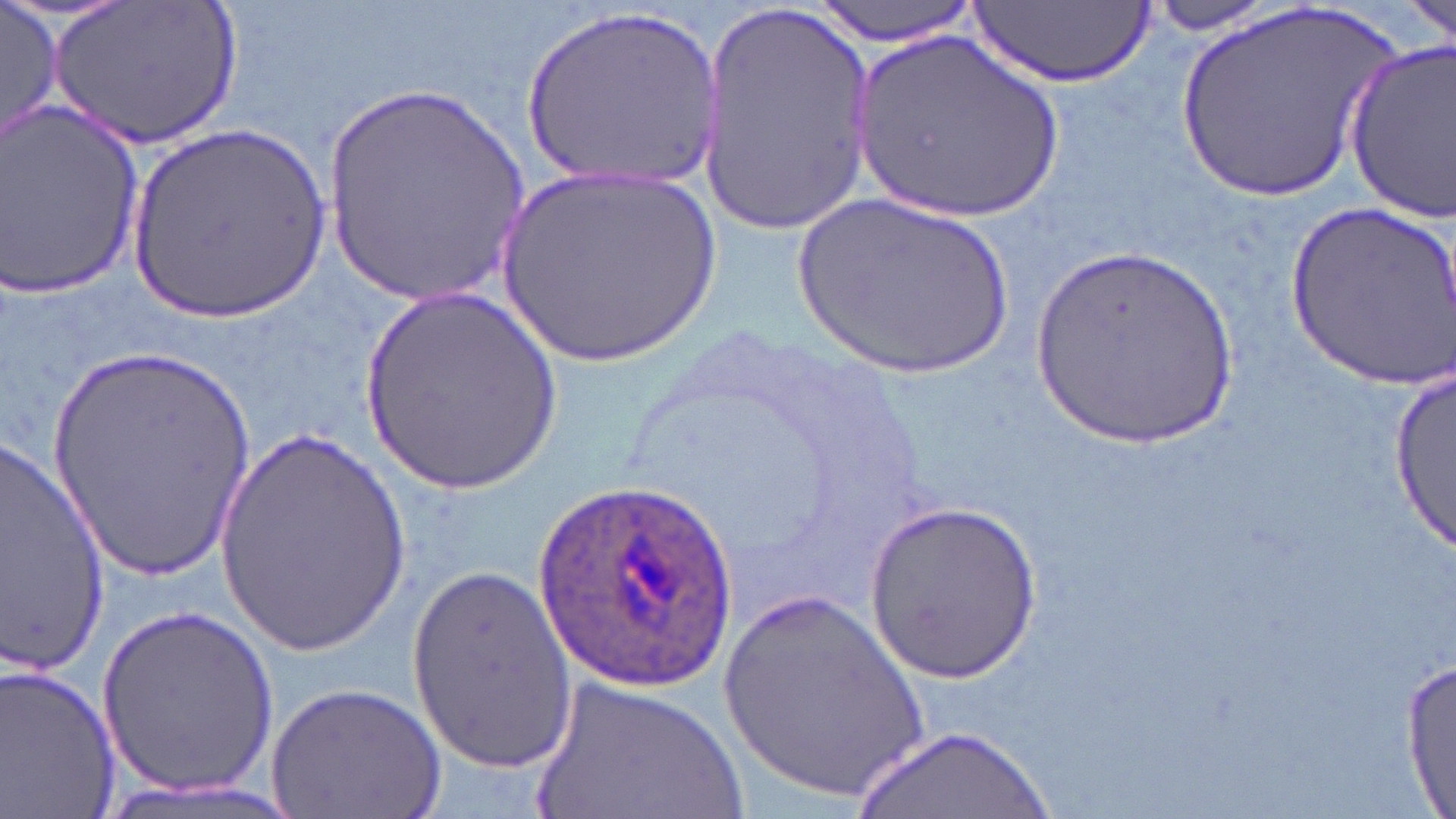
Summary:
  - Coordinate format: approximate bounding boxes as [x1, y1, x2, y2] in pixels
  - Plasmodium ovale-infected red blood cell locations: [535, 480, 740, 692]
  - Uninfected red blood cell locations: [2, 0, 62, 146], [47, 0, 241, 153], [808, 0, 984, 44], [1144, 0, 1298, 33], [1405, 0, 1454, 47], [971, 2, 1152, 87], [696, 4, 880, 232], [1171, 4, 1406, 210], [515, 5, 725, 196], [852, 30, 1068, 225], [1344, 38, 1456, 225], [319, 87, 530, 306], [1, 102, 148, 304], [126, 119, 335, 321], [487, 165, 728, 366], [786, 190, 1021, 385], [1287, 198, 1456, 388], [1028, 245, 1248, 454], [359, 284, 561, 498], [45, 342, 260, 586], [1391, 355, 1453, 562], [210, 422, 415, 657], [1, 430, 108, 677], [865, 499, 1041, 679], [406, 566, 576, 774], [715, 583, 933, 804], [100, 601, 278, 797], [1402, 660, 1455, 814], [0, 661, 123, 819], [527, 675, 753, 819], [264, 681, 447, 819], [857, 726, 1053, 819]
  - Slide-level diagnosis: Plasmodium ovale
  - Preparation: thin blood film
  - Magnification: 1000x
  - Field of view: single
  - Modality: optical microscopy
  - Stain: May-Grünwald-Giemsa
  - Image size: 1456×819 pixels